Identify the parasite.
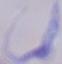
This is a trypanosome.

Summary:
  - Magnification: 1000x
  - Modality: micrograph